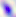
Summary:
  - Magnification: 400x
  - Modality: micrograph
  - Identification: Toxoplasma gondii